Locate every malaria parasite and every leukocyte.
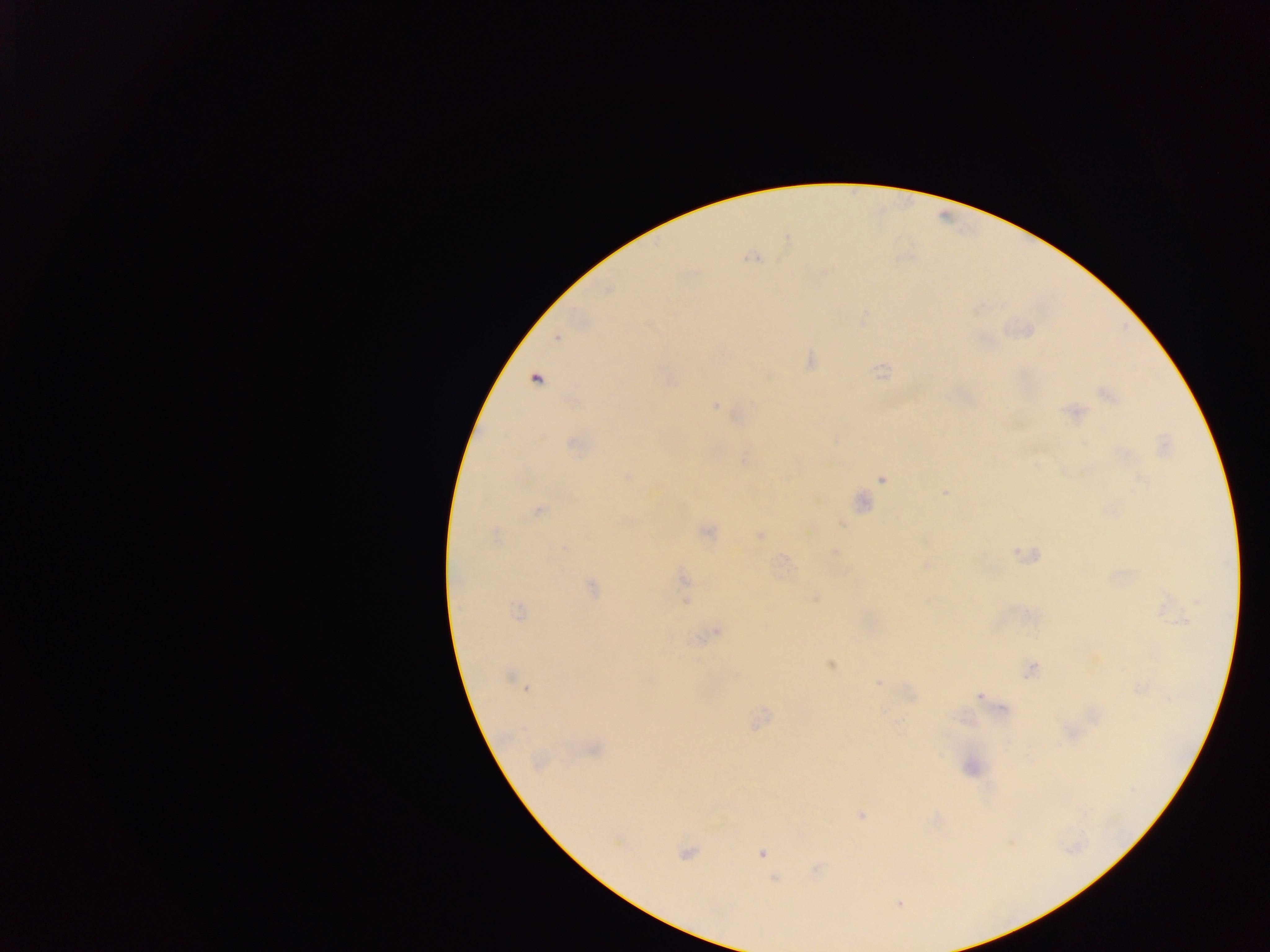

Approximate centers as [x, y] in pixels.
Malaria parasites: [787, 238], [753, 257], [557, 337], [811, 360], [882, 371], [769, 375], [535, 379], [1108, 395], [715, 406], [1073, 411], [574, 443], [745, 457], [627, 476], [883, 477], [945, 492], [861, 502], [537, 510], [707, 532], [759, 535], [495, 537], [834, 553], [1026, 554], [926, 564], [683, 580], [591, 588], [815, 597], [518, 611], [716, 630], [830, 663], [1030, 670], [513, 680], [878, 682], [525, 687], [1139, 687], [978, 695], [759, 720], [592, 749], [971, 767], [861, 815], [685, 852], [762, 852], [816, 868], [774, 879], [899, 903].
No leukocytes observed.

Sample from Ghana. Mobile-phone photograph taken through the microscope. Thick blood smear. Single field of view. Image is 1270×952 pixels.